Assess the morphology of the erythrocytes.
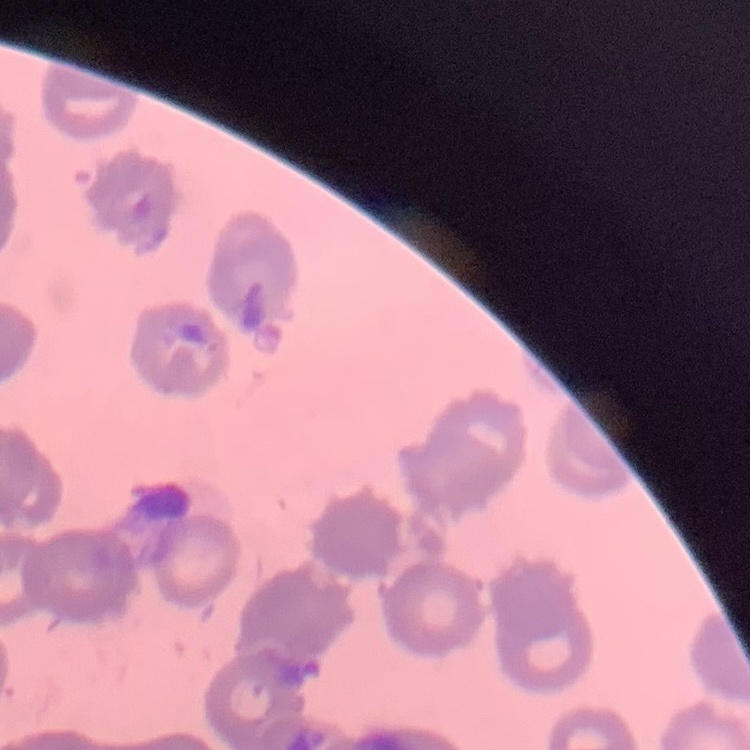

Rouleaux formation.

One tile cut from a larger photomicrograph. Thin blood smear. Field's or Giemsa stain.